Report the malaria status of this cell.
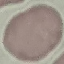
Uninfected.

Summary:
  - Stain: Giemsa
  - Capture: smartphone through the microscope eyepiece
  - Preparation: thin smear
  - Image type: automatically extracted cell patch, resized to 64 × 64 pixels